Give the extent of all Plasmodium falciparum-infected red blood cells.
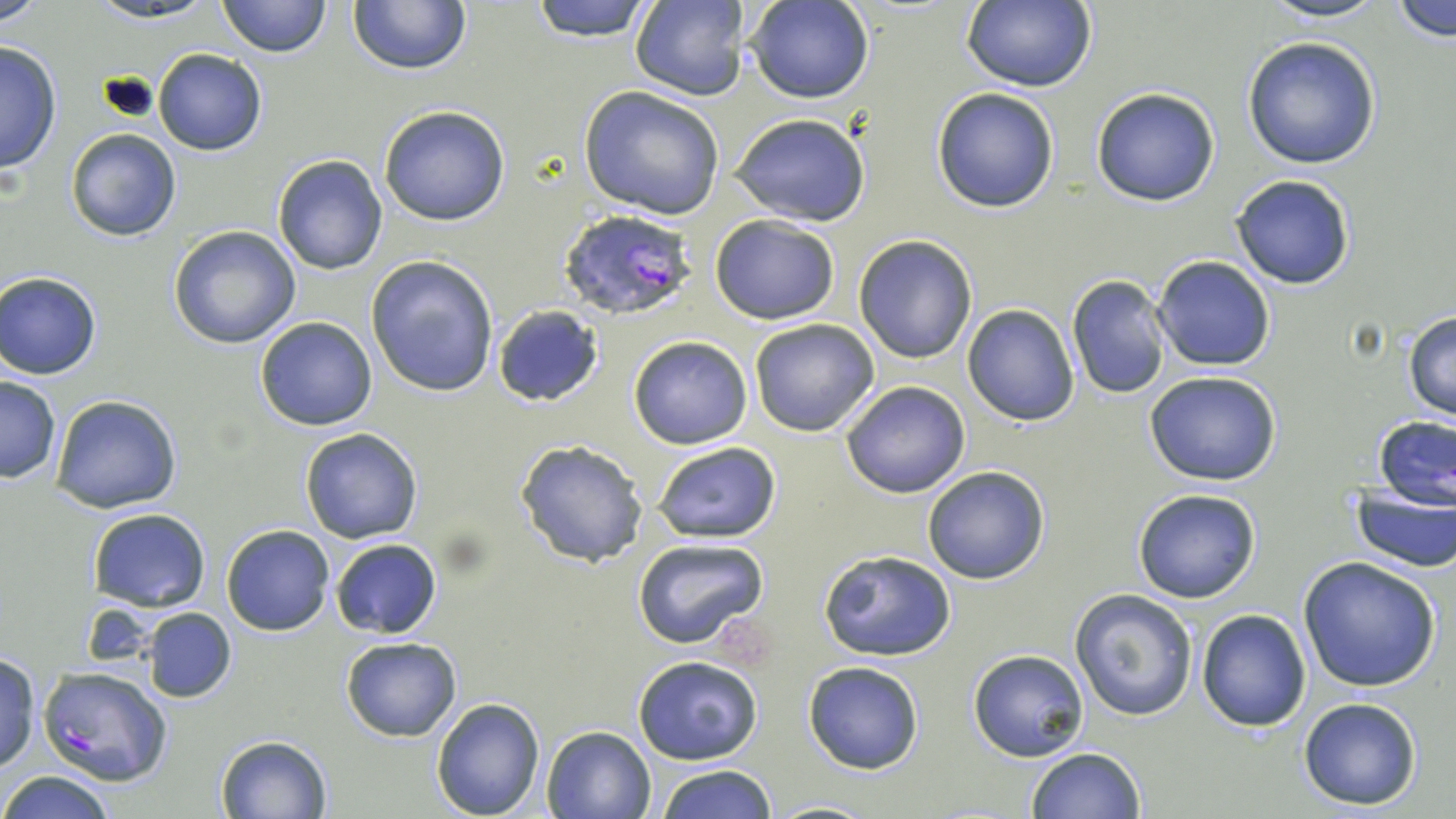
Approximate bounding boxes as (x1, y1, x2, y2) in pixels.
Plasmodium falciparum-infected red blood cells: (558, 208, 699, 321), (37, 664, 172, 787).

Uninfected red blood cell locations: (0, 0, 45, 27), (84, 0, 227, 24), (216, 0, 332, 57), (530, 0, 656, 42), (630, 0, 748, 101), (748, 0, 873, 104), (1260, 0, 1388, 24), (348, 1, 471, 75), (959, 1, 1097, 92), (1390, 2, 1455, 45), (1242, 36, 1381, 169), (0, 39, 61, 177), (153, 48, 268, 156), (579, 85, 726, 220), (1090, 87, 1222, 207), (931, 88, 1059, 212), (378, 104, 512, 226), (729, 110, 872, 227), (65, 129, 181, 241), (273, 154, 387, 274), (1229, 174, 1355, 290), (709, 214, 840, 324), (169, 226, 301, 350), (853, 235, 979, 363), (366, 255, 499, 398), (1150, 256, 1276, 371), (1, 272, 103, 379), (1066, 274, 1170, 399), (491, 304, 605, 408), (962, 304, 1080, 425), (1403, 310, 1456, 422), (254, 316, 377, 431), (750, 318, 879, 437), (628, 335, 752, 450), (1143, 370, 1283, 486), (1, 376, 61, 484), (839, 381, 970, 499), (50, 394, 184, 513), (1373, 416, 1456, 510), (300, 426, 424, 544), (514, 439, 648, 570), (652, 441, 780, 546), (921, 465, 1052, 585), (1347, 486, 1456, 571), (1132, 490, 1261, 604), (87, 507, 212, 611), (221, 524, 334, 636), (330, 538, 442, 639), (630, 539, 772, 651), (819, 549, 957, 661), (1297, 555, 1442, 692), (1070, 589, 1199, 722), (1196, 608, 1311, 731), (143, 609, 236, 702), (340, 637, 462, 741), (967, 649, 1090, 761), (1, 655, 40, 773), (633, 656, 763, 765), (803, 661, 925, 774), (1298, 697, 1423, 809), (430, 698, 546, 818), (541, 726, 656, 818), (216, 734, 331, 817), (1023, 747, 1147, 819), (653, 764, 780, 819), (0, 771, 119, 818), (764, 799, 881, 817). Slide-level diagnosis: Plasmodium falciparum. One field of a larger specimen. Image is 1456×819 pixels. Optical microscopy. Thin blood smear. 1000x magnification. May-Grünwald-Giemsa-stained preparation.